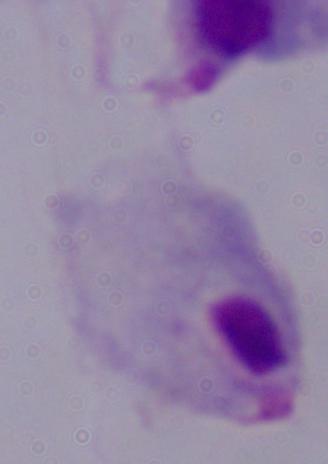
{
  "modality": "photomicrograph",
  "identification": "trichomonad",
  "magnification": "1000x"
}